Classify the preparation.
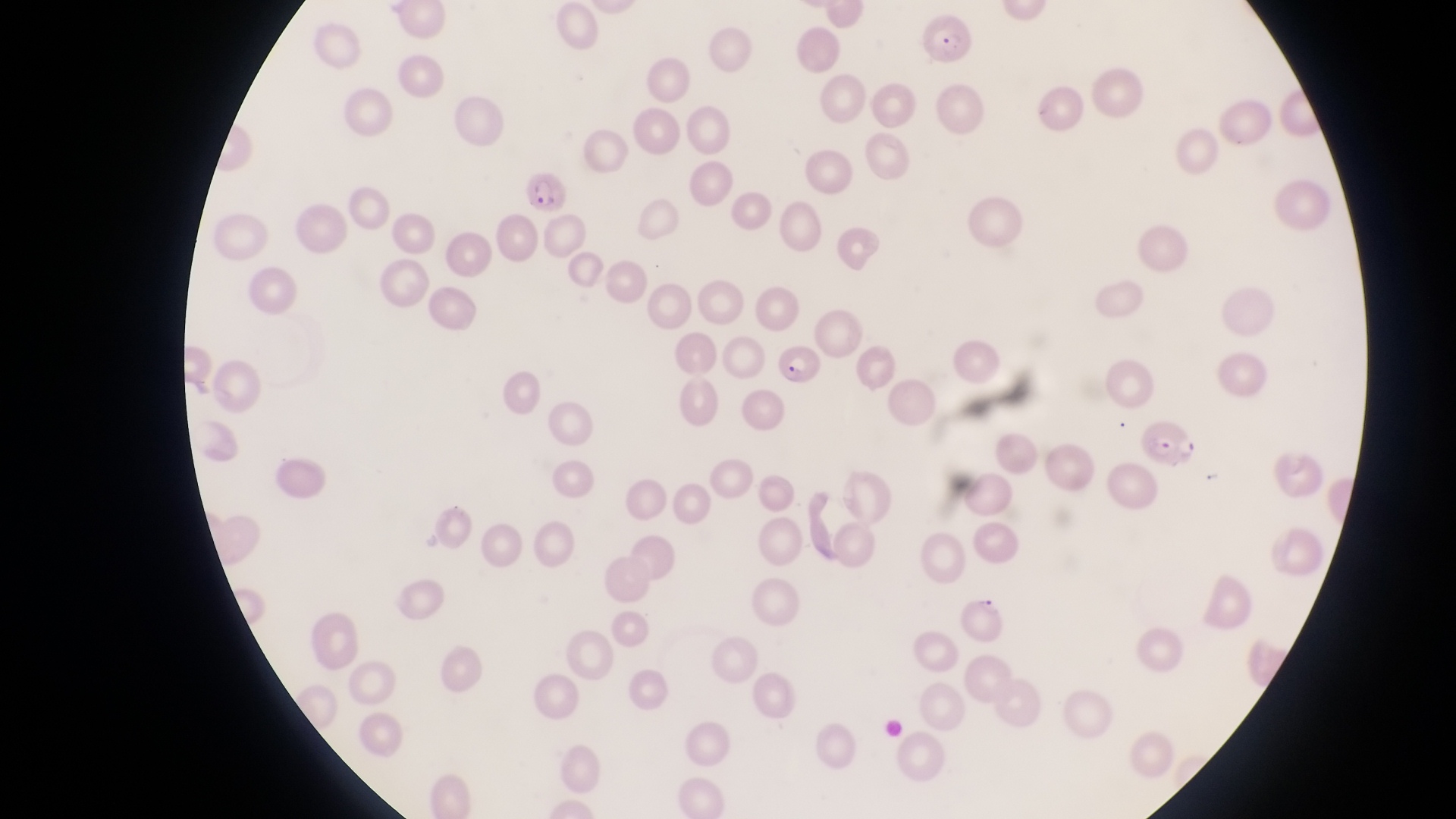

Thin blood film.

capture = smartphone photograph through the eyepiece of an Olympus CX-23 microscope
image size = 1456×819 pixels
parasitised red blood cell locations = approximate bounding boxes as {left, top, right, bottom} in pixels: {918, 10, 977, 69}, {518, 171, 568, 217}, {774, 340, 826, 392}, {1141, 412, 1201, 470}, {952, 591, 1018, 649}
magnification = 1000x
country = Uganda
field of view = single